Give the extent of all Plasmodium ovale-infected red blood cells.
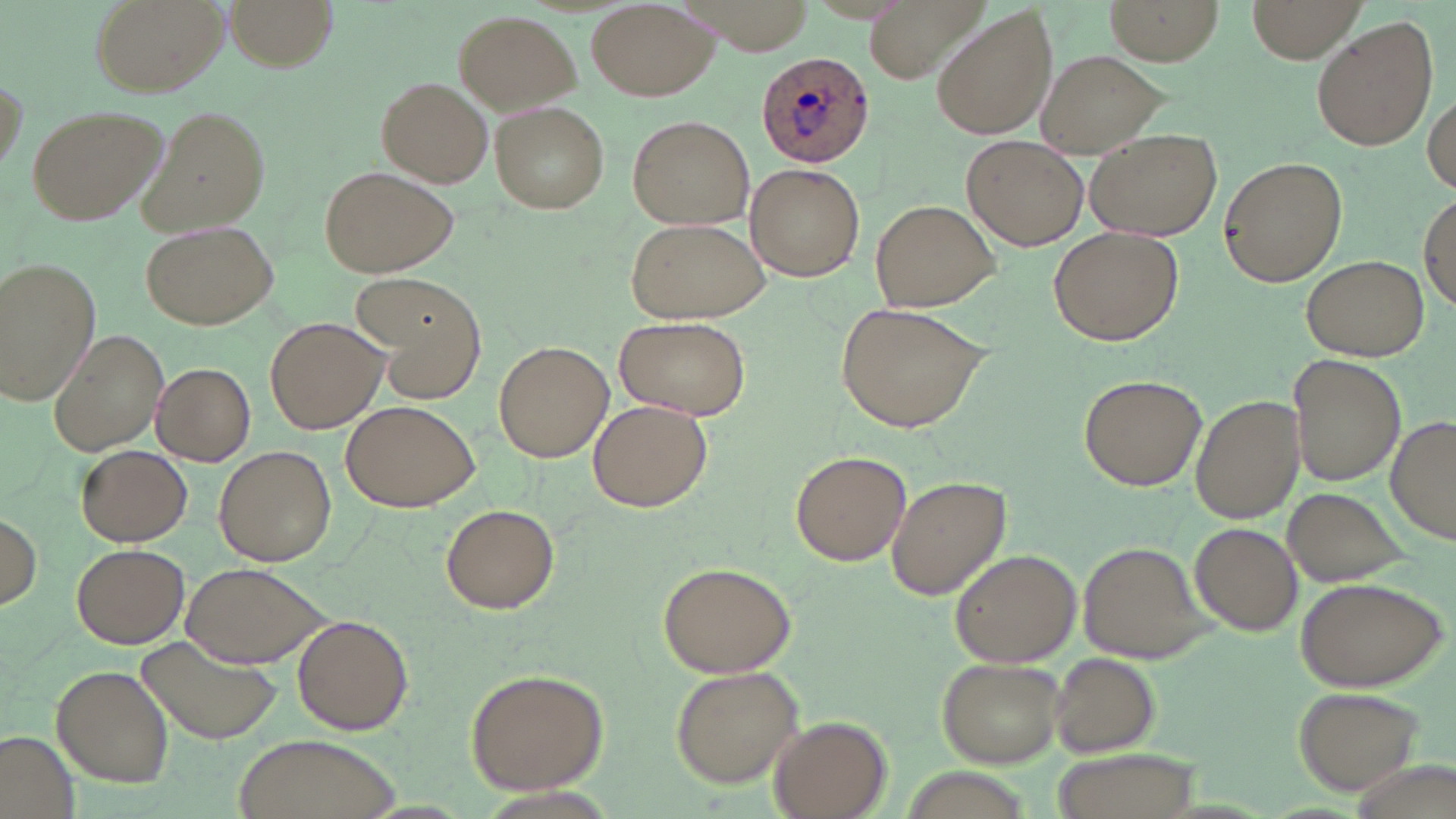

Approximate bounding boxes as [x1, y1, x2, y2] in pixels.
Plasmodium ovale-infected red blood cells: [755, 49, 876, 168].

slide_level_diagnosis: Plasmodium ovale
uninfected_red_blood_cell_locations: 'approximate bounding boxes as [x1, y1, x2, y2] in pixels: [88, 0, 227, 98], [225, 0, 337, 70], [1104, 0, 1224, 65], [1247, 0, 1366, 62], [587, 2, 718, 101], [929, 7, 1059, 143], [452, 9, 581, 114], [1312, 19, 1439, 153], [1036, 50, 1168, 158], [377, 77, 494, 188], [1426, 89, 1456, 195], [493, 102, 609, 212], [139, 103, 273, 235], [28, 105, 168, 225], [627, 113, 753, 230], [1085, 132, 1222, 241], [963, 137, 1091, 251], [1218, 157, 1348, 287], [744, 162, 866, 281], [320, 165, 460, 277], [1418, 190, 1455, 313], [870, 199, 1000, 312], [625, 216, 771, 325], [141, 219, 279, 330], [1049, 227, 1183, 345], [1301, 254, 1428, 361], [2, 257, 102, 405], [357, 270, 488, 403], [837, 303, 990, 432], [264, 315, 388, 434], [615, 316, 750, 419], [48, 326, 170, 456], [493, 341, 613, 463], [1288, 353, 1405, 487], [152, 363, 255, 465], [1078, 374, 1206, 492], [1191, 393, 1304, 524], [588, 398, 713, 512], [340, 399, 478, 513], [1386, 414, 1456, 546], [76, 444, 192, 547], [213, 445, 337, 566], [790, 450, 910, 567], [884, 474, 1011, 600], [1281, 484, 1415, 588], [442, 503, 560, 613], [0, 513, 43, 612], [1192, 522, 1302, 637], [72, 543, 189, 649], [1079, 543, 1203, 660], [950, 548, 1081, 667], [182, 561, 330, 669], [656, 561, 798, 678], [1294, 576, 1447, 691], [292, 614, 414, 734], [140, 633, 284, 744], [1051, 652, 1161, 756], [938, 656, 1064, 766], [52, 664, 173, 789], [671, 665, 805, 786], [464, 666, 609, 794], [1293, 685, 1429, 798], [770, 715, 891, 818], [1, 732, 80, 819], [229, 732, 405, 819], [1045, 748, 1203, 819]'
field_of_view: one of a larger specimen
image_size: 1456×819 pixels
stain: May-Grünwald-Giemsa
magnification: 1000x
preparation: thin blood film
modality: light microscopy